Outline each blood parasite and name the species.
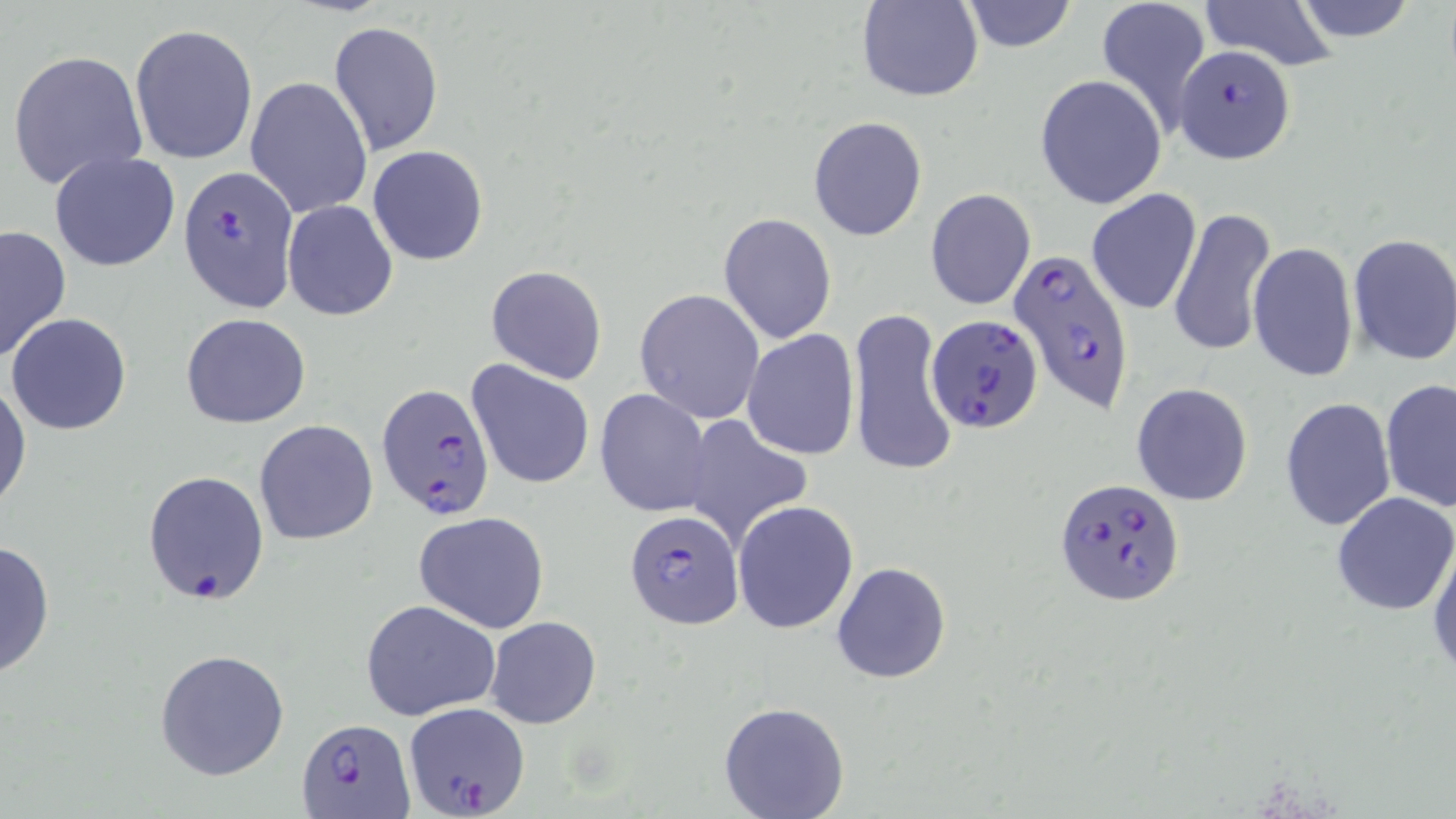
Approximate bounding boxes as [x1, y1, x2, y2] in pixels.
Plasmodium falciparum-infected red blood cells: [1175, 43, 1294, 164], [176, 166, 296, 312], [1008, 251, 1134, 417], [926, 314, 1044, 434], [378, 382, 495, 518], [1055, 477, 1184, 606], [625, 509, 743, 631], [403, 702, 531, 817], [297, 718, 410, 817].
No Plasmodium ovale, Plasmodium malariae, Plasmodium vivax, Babesia divergens, or Trypanosoma brucei observed.

Uninfected red blood cell locations: [858, 0, 982, 102], [1094, 0, 1212, 135], [1195, 0, 1340, 69], [960, 1, 1077, 52], [1289, 1, 1422, 45], [329, 20, 443, 153], [129, 24, 258, 164], [7, 48, 149, 191], [1035, 74, 1167, 210], [245, 76, 372, 218], [808, 116, 928, 240], [369, 146, 489, 265], [48, 151, 181, 273], [925, 187, 1036, 310], [1087, 188, 1201, 316], [282, 201, 397, 321], [1168, 207, 1275, 359], [717, 213, 837, 343], [0, 225, 71, 362], [1346, 233, 1456, 366], [1248, 243, 1360, 382], [485, 265, 606, 384], [634, 288, 765, 423], [848, 307, 959, 479], [6, 313, 132, 436], [181, 313, 311, 428], [741, 328, 860, 461], [467, 359, 595, 490], [0, 373, 31, 515], [1380, 378, 1456, 513], [1131, 382, 1253, 506], [594, 389, 714, 518], [1280, 397, 1397, 532], [678, 413, 814, 548], [255, 420, 380, 545], [142, 470, 270, 607], [1330, 491, 1456, 616], [732, 500, 859, 635], [413, 511, 550, 632], [1427, 533, 1456, 680], [0, 536, 56, 680], [831, 562, 952, 683], [359, 598, 501, 720], [484, 615, 602, 730], [155, 648, 292, 781], [718, 700, 849, 819]. Slide-level diagnosis: Plasmodium falciparum. One field of a larger specimen. 1000x magnification. May-Grünwald-Giemsa-stained preparation. Image is 1456×819 pixels. Thin blood smear. Optical microscopy.